Assess this cell for malaria.
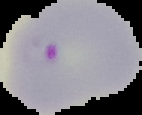
It is parasitized.

Summary:
  - Image size: 142×115 pixels
  - Image type: segmented cell region with the area outside set to black
  - Preparation: thin blood smear